Point out each leukocyte.
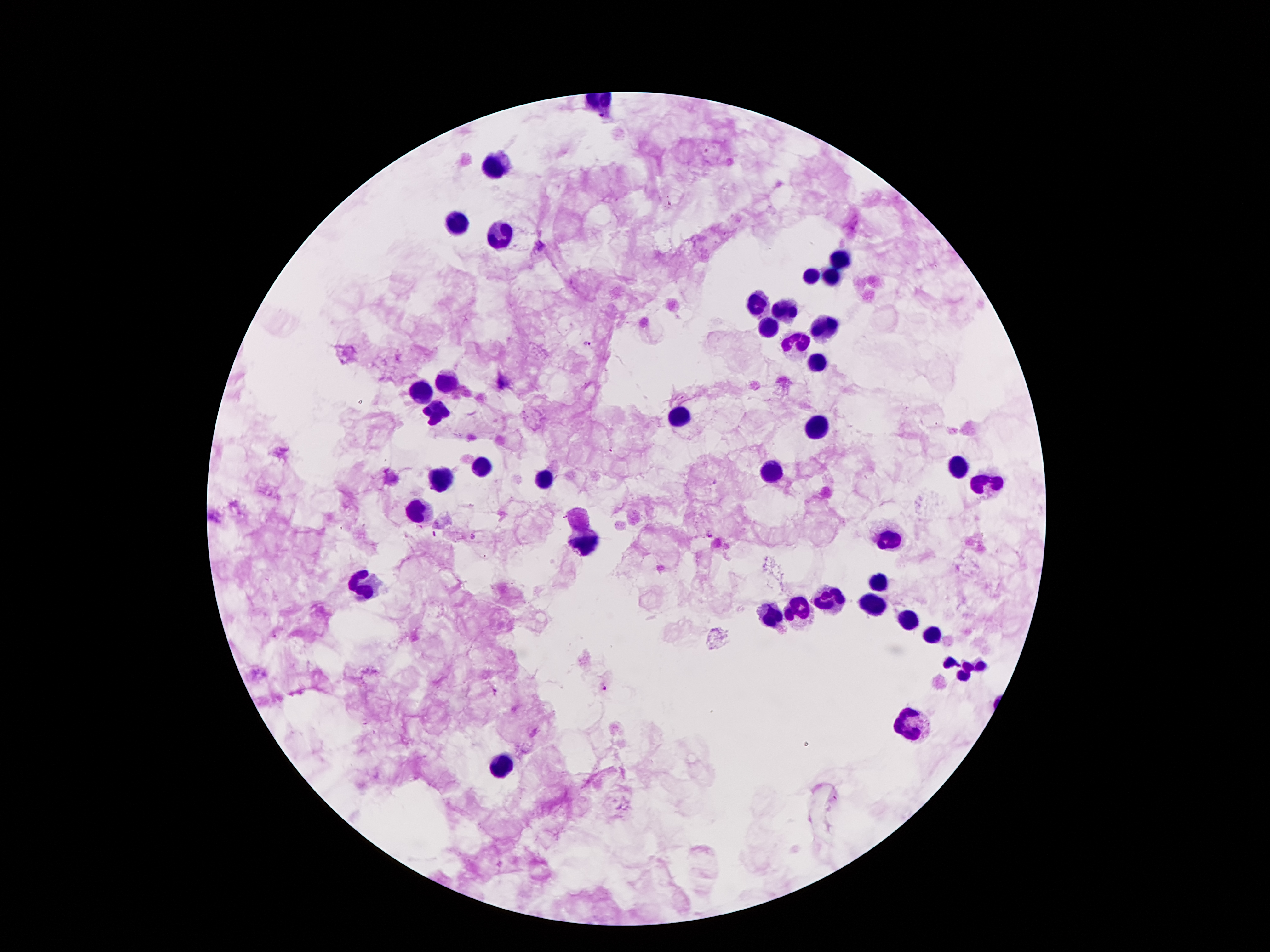
Approximate object centers, in pixels from the top-left corner.
Leukocytes: (x=495, y=166), (x=454, y=222), (x=498, y=235), (x=839, y=260), (x=811, y=275), (x=830, y=276), (x=760, y=303), (x=782, y=310), (x=768, y=327), (x=820, y=329), (x=798, y=343), (x=817, y=363), (x=449, y=381), (x=421, y=392), (x=437, y=414), (x=679, y=416), (x=817, y=425), (x=953, y=465), (x=481, y=467), (x=773, y=470), (x=541, y=477), (x=441, y=480), (x=988, y=485), (x=418, y=511), (x=580, y=518), (x=890, y=540), (x=584, y=543), (x=879, y=581), (x=362, y=586), (x=834, y=601), (x=873, y=601), (x=798, y=609), (x=771, y=616), (x=907, y=620), (x=931, y=637), (x=966, y=666), (x=912, y=726), (x=498, y=769).

Malaria parasite locations: (x=604, y=116), (x=707, y=151), (x=587, y=344), (x=612, y=450), (x=716, y=483), (x=565, y=516), (x=434, y=534), (x=709, y=534), (x=473, y=537), (x=605, y=688), (x=494, y=692). 100x magnification. Thick peripheral-blood smear. Image is 1270×952 pixels. One field from this slide. Giemsa-stained preparation. Patient malaria status: infected with Plasmodium falciparum. Photographed through the microscope eyepiece with a smartphone camera.